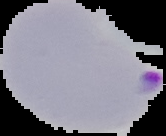
result = malaria parasites identified
image type = segmented cell region with the area outside set to black
preparation = thin blood smear
image size = 166×136 pixels